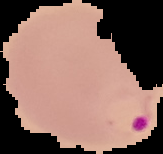 From a thin blood smear. Image is 163×154 pixels. Segmented cell region on a black background. Malaria status: parasitized.